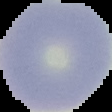
From a thin blood film. Malaria status: uninfected. Image is 112×112 pixels. Segmented cell region on a black background.